Identify the parasite.
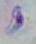

This is Toxoplasma gondii.

magnification: 1000x
modality: micrograph